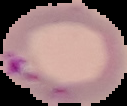 From a thin blood film. Cell region segmented out of the field of view; the surrounding area is masked to black. Image is 127×106 pixels. Result: malaria parasites detected.